Locate every blood parasite and identify its species.
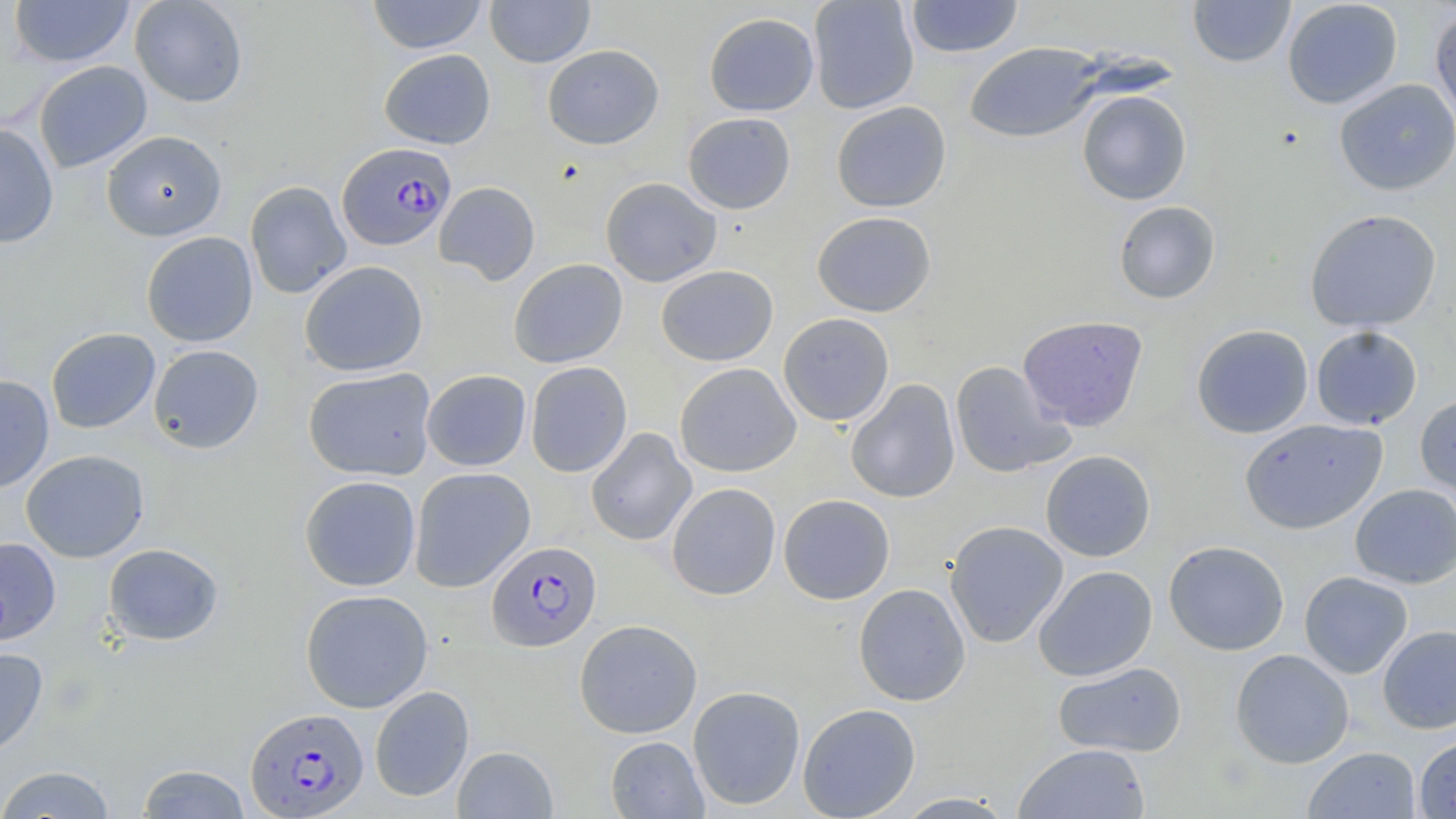

Approximate bounding boxes as (x1, y1, x2, y2) in pixels.
Plasmodium falciparum-infected red blood cells: (337, 142, 456, 251), (486, 541, 601, 652), (245, 706, 368, 817).
No Plasmodium ovale, Plasmodium malariae, Plasmodium vivax, Babesia divergens, or Trypanosoma brucei observed.

Uninfected red blood cell locations: (8, 0, 134, 68), (130, 0, 248, 107), (367, 0, 488, 54), (485, 0, 595, 67), (808, 0, 920, 114), (904, 0, 1024, 58), (1188, 0, 1295, 67), (1282, 0, 1403, 109), (1430, 7, 1456, 127), (704, 12, 819, 117), (964, 42, 1103, 143), (542, 44, 664, 150), (379, 49, 496, 149), (33, 60, 152, 173), (1334, 79, 1456, 196), (1077, 89, 1192, 205), (831, 101, 952, 213), (682, 112, 796, 214), (0, 122, 59, 248), (101, 130, 227, 241), (600, 177, 722, 287), (244, 180, 352, 299), (434, 181, 541, 286), (1113, 201, 1221, 304), (1304, 209, 1442, 333), (812, 211, 936, 317), (141, 231, 259, 347), (508, 258, 628, 368), (300, 261, 428, 377), (656, 265, 778, 366), (778, 313, 895, 426), (1017, 315, 1148, 431), (1191, 324, 1313, 439), (1310, 326, 1422, 430), (46, 328, 160, 433), (148, 344, 264, 453), (525, 361, 632, 478), (950, 361, 1074, 478), (674, 363, 801, 477), (303, 367, 437, 481), (422, 369, 531, 471), (0, 374, 54, 493), (846, 379, 960, 503), (1415, 393, 1456, 510), (1240, 418, 1387, 534), (585, 427, 696, 546), (21, 449, 149, 563), (1040, 450, 1156, 562), (409, 466, 536, 592), (300, 475, 421, 591), (666, 482, 781, 600), (1350, 483, 1456, 588), (778, 494, 895, 604), (944, 520, 1069, 648), (0, 537, 61, 646), (1164, 540, 1289, 656), (103, 543, 224, 645), (1033, 565, 1158, 682), (1299, 571, 1413, 679), (853, 583, 971, 706), (300, 589, 434, 713), (574, 619, 702, 739), (1377, 625, 1456, 734), (0, 647, 48, 761), (1230, 649, 1354, 768), (1052, 661, 1187, 758), (369, 685, 474, 802), (687, 685, 805, 810), (797, 702, 921, 819), (1414, 734, 1456, 818), (605, 736, 709, 818), (1013, 743, 1149, 819), (452, 745, 558, 818), (1303, 746, 1420, 818), (135, 763, 252, 819), (0, 765, 118, 818), (894, 792, 1016, 818). Slide-level diagnosis: Plasmodium falciparum. One field of a larger specimen. May-Grünwald-Giemsa-stained preparation. 1000x magnification. Optical microscopy. Thin blood smear. Image is 1456×819 pixels.